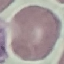
Malaria status: uninfected. Thin smear of blood. Cell patch, automatically extracted from a larger field of view and resized to 64 × 64 pixels. Giemsa stain. Photographed with a smartphone camera at the microscope eyepiece.